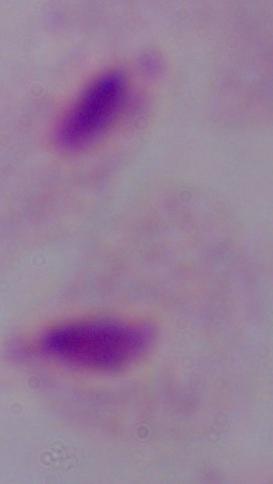

Summary:
  - Identification: trichomonad
  - Modality: photomicrograph
  - Magnification: 1000x